Assess this cell for malaria.
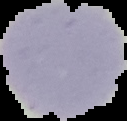

Uninfected.

image size = 127×121 pixels
image type = cell region segmented out of the field of view; surrounding area masked to black
preparation = thin blood film